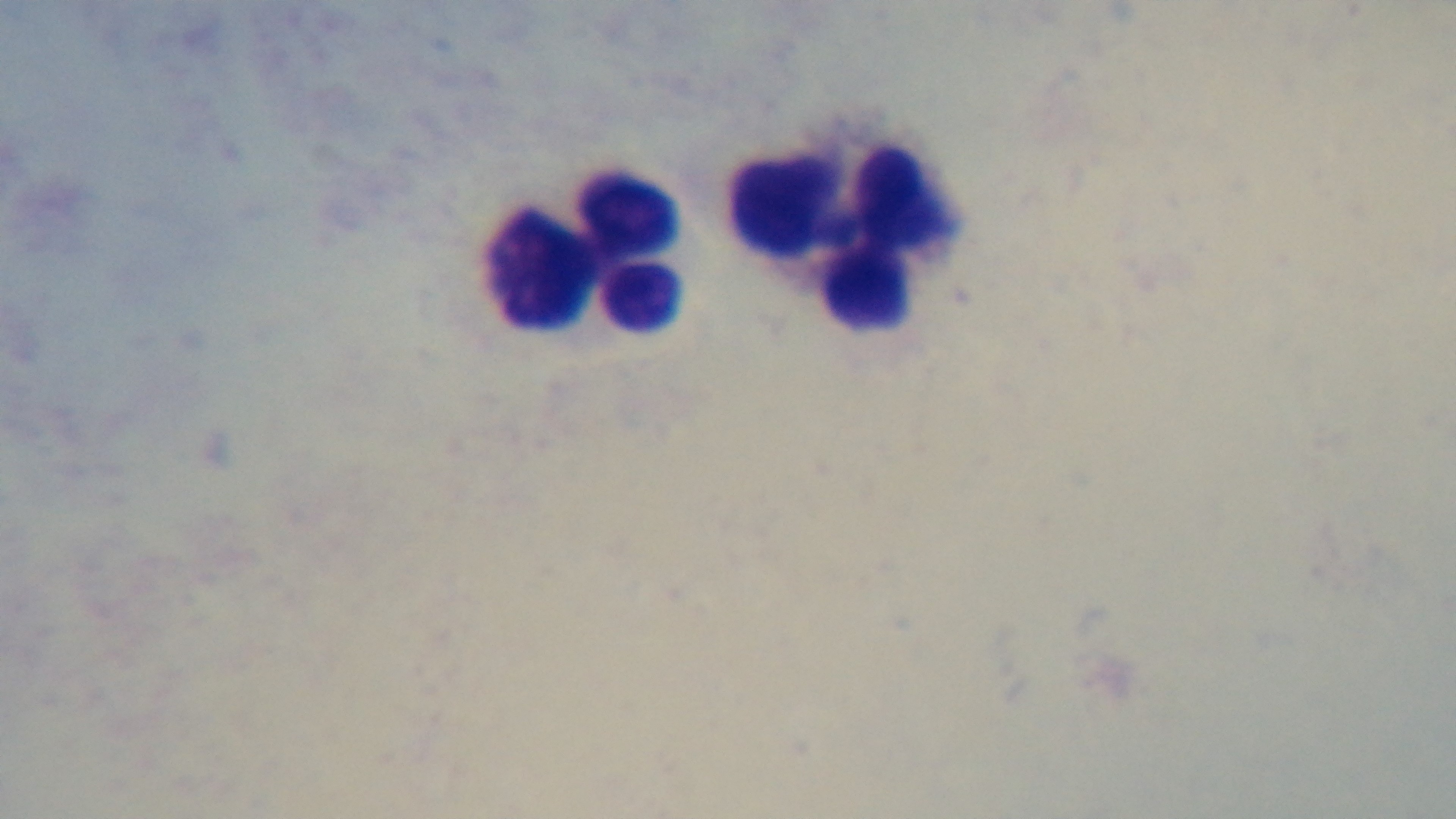

Summary:
  - Modality: light microscopy
  - Preparation: thick smear
  - Stain: Giemsa
  - Field of view: one from the slide
  - Objective: 100x oil immersion
  - Capture: mounted 4K digital camera
  - Malaria status: uninfected